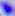
Summary:
  - Modality: photomicrograph
  - Identification: Toxoplasma gondii
  - Magnification: 400x